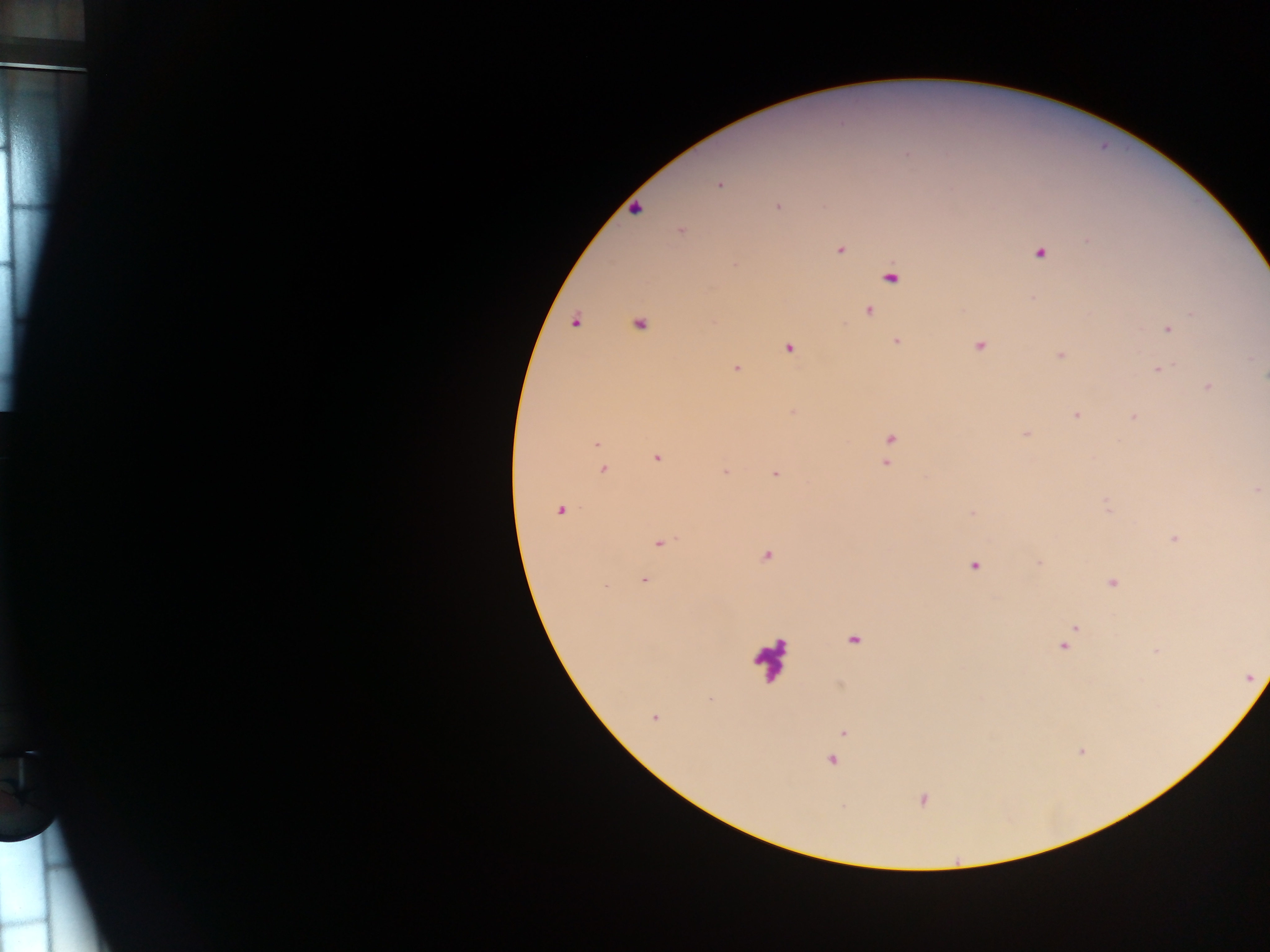

preparation = thick blood film
capture = mobile-phone photograph through a microscope
Plasmodium parasite locations = approximate centers as [x, y] in pixels: [720, 184], [778, 207], [636, 210], [681, 230], [839, 250], [1040, 253], [890, 277], [869, 310], [1192, 314], [576, 321], [638, 325], [1168, 328], [897, 342], [980, 346], [788, 348], [1061, 356], [1250, 358], [736, 368], [1159, 370], [1207, 387], [1077, 414], [1133, 418], [1027, 435], [890, 439], [597, 443], [658, 458], [887, 463], [603, 470], [725, 472], [775, 474], [1256, 490], [1107, 505], [560, 510], [972, 512], [1174, 539], [660, 543], [766, 556], [1039, 563], [974, 566], [644, 580], [1112, 583], [604, 586], [1074, 630], [854, 639], [1064, 645], [1155, 651], [709, 699], [654, 717], [844, 732], [832, 761], [923, 800]
field of view = single
country = Ghana
image size = 1270×952 pixels
leukocyte locations = approximate centers as [x, y] in pixels: [769, 660]